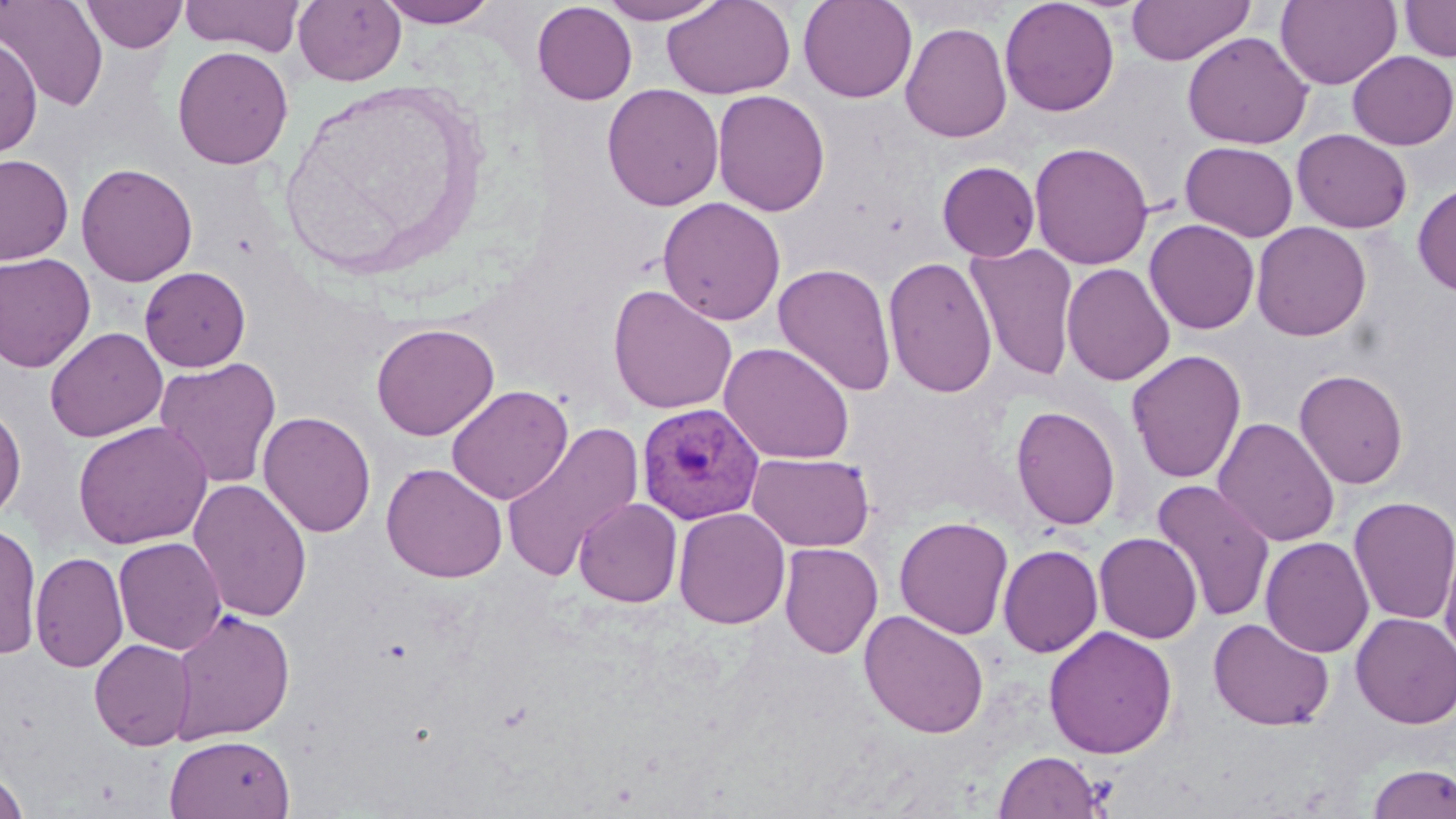
Summary:
  - Coordinate format: approximate bounding boxes as (x1, y1, x2, y2) in pixels
  - Uninfected red blood cell locations: (0, 0, 109, 111), (80, 0, 188, 53), (179, 0, 305, 56), (293, 0, 406, 86), (376, 0, 501, 27), (596, 0, 727, 24), (798, 0, 918, 103), (999, 0, 1120, 117), (1125, 0, 1255, 66), (1275, 0, 1401, 89), (1399, 0, 1456, 62), (661, 1, 796, 99), (532, 2, 637, 105), (900, 21, 1013, 143), (1182, 31, 1313, 149), (0, 37, 41, 158), (172, 45, 293, 170), (1347, 50, 1456, 150), (602, 83, 724, 211), (712, 89, 831, 217), (1292, 129, 1413, 233), (1029, 141, 1153, 270), (1181, 141, 1298, 242), (0, 153, 74, 265), (937, 161, 1040, 262), (76, 163, 198, 286), (1413, 182, 1456, 296), (658, 197, 786, 325), (1144, 219, 1260, 335), (1251, 221, 1371, 341), (965, 243, 1080, 381), (0, 252, 96, 373), (883, 255, 998, 398), (774, 262, 897, 397), (1061, 263, 1175, 386), (140, 266, 251, 372), (608, 284, 737, 415), (371, 322, 499, 441), (45, 326, 167, 443), (719, 342, 855, 465), (1126, 349, 1247, 485), (153, 357, 282, 490), (1294, 369, 1410, 489), (445, 385, 574, 504), (0, 402, 27, 524), (1010, 404, 1121, 531), (258, 410, 376, 538), (1213, 416, 1340, 547), (72, 421, 213, 550), (500, 422, 644, 585), (747, 452, 874, 551), (381, 462, 508, 583), (189, 479, 313, 623), (1151, 479, 1276, 622), (1348, 496, 1456, 625), (574, 497, 683, 608), (673, 507, 791, 629), (894, 516, 1014, 639), (0, 521, 42, 660), (1439, 531, 1456, 663), (1094, 532, 1202, 644), (1260, 535, 1374, 658), (113, 536, 227, 655), (779, 542, 883, 659), (998, 544, 1103, 658), (30, 551, 128, 673), (168, 608, 294, 745), (859, 609, 989, 739), (1351, 612, 1456, 729), (1208, 617, 1334, 731), (1042, 625, 1178, 759), (89, 639, 196, 750), (164, 734, 294, 819), (993, 750, 1104, 818), (1367, 763, 1456, 819), (0, 769, 30, 818)
  - Plasmodium vivax-infected red blood cell locations: (636, 402, 764, 524)
  - Slide-level diagnosis: Plasmodium vivax
  - Stain: May-Grünwald-Giemsa
  - Preparation: thin blood smear
  - Field of view: single
  - Modality: light microscopy
  - Magnification: 1000x
  - Image size: 1456×819 pixels